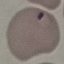 Malaria status: parasitized. Giemsa-stained preparation. Thin smear of blood. Photographed with a smartphone camera at the microscope eyepiece. Cell patch, automatically extracted from a larger field of view and resized to 64 × 64 pixels.